Comment on the morphology of the red blood cells.
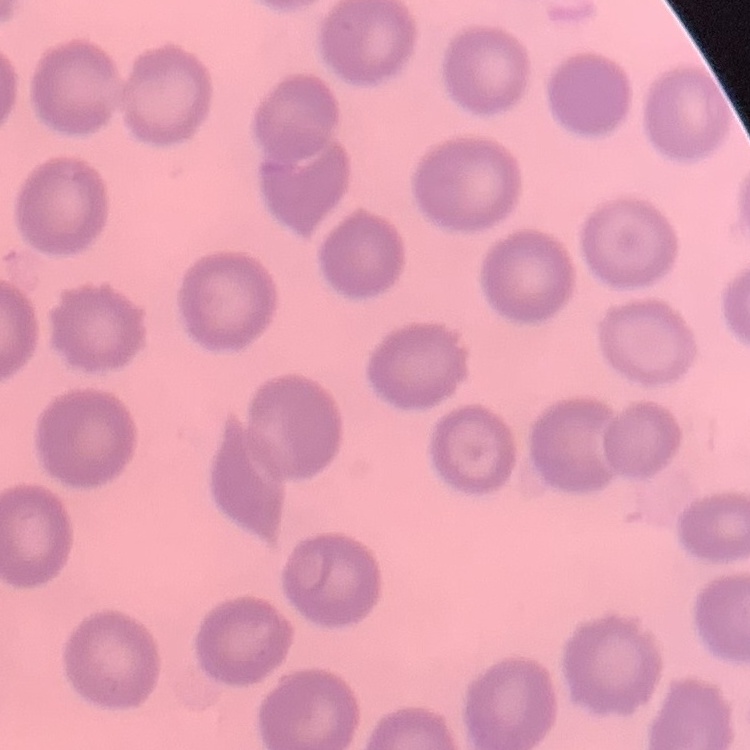
No rouleaux formation.

Thin blood smear. Square crop of a larger photomicrograph. Stained with either Field's or Giemsa.